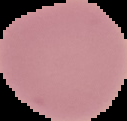

Cell region segmented out of the field of view; the surrounding area is masked to black. From a thin blood film. Image is 127×121 pixels. Result: no malaria parasites detected.